Name the cell type shown.
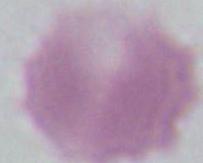

This is an erythrocyte.

Captured at 1000x magnification. Photomicrograph.